Classify this cell by malaria status.
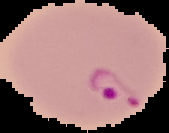

It is parasitized.

preparation = thin blood film
image type = segmented cell region with the area outside set to black
image size = 169×133 pixels